Locate cells.
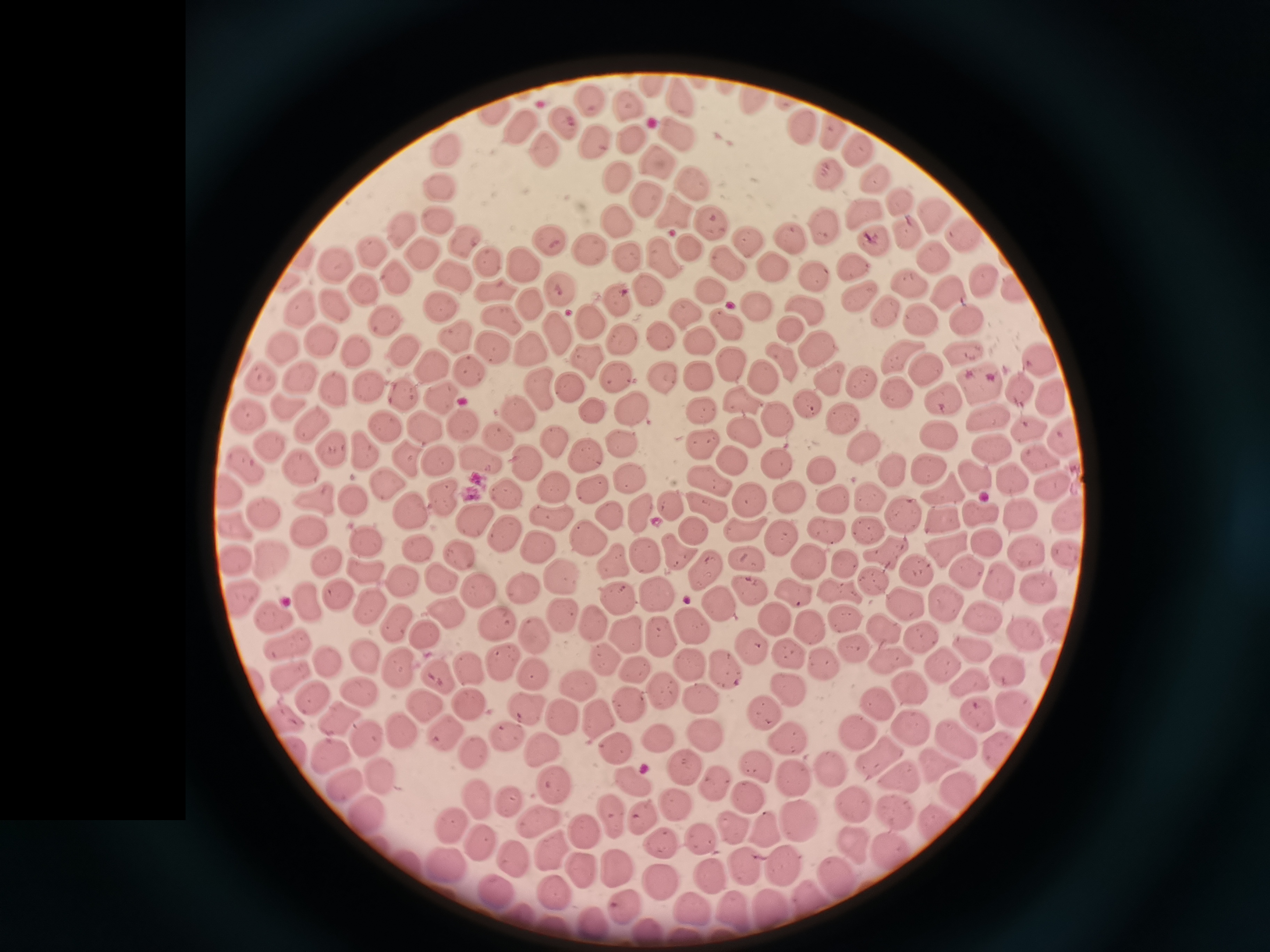

Approximate object centers, in pixels from the top-left corner.
Cells: (x=650, y=89), (x=684, y=99), (x=755, y=99), (x=594, y=104), (x=629, y=107), (x=493, y=111), (x=564, y=124), (x=521, y=125), (x=803, y=127), (x=833, y=132), (x=677, y=134), (x=633, y=137), (x=599, y=143), (x=856, y=150), (x=548, y=153), (x=444, y=156), (x=652, y=161), (x=828, y=174), (x=616, y=179), (x=875, y=180), (x=694, y=182), (x=439, y=190), (x=653, y=201), (x=898, y=201), (x=863, y=212), (x=675, y=213), (x=930, y=214), (x=438, y=222), (x=615, y=222), (x=710, y=223), (x=398, y=228), (x=828, y=228), (x=790, y=234), (x=964, y=234), (x=904, y=236), (x=459, y=241), (x=547, y=242), (x=749, y=242), (x=870, y=246), (x=686, y=247), (x=587, y=248), (x=369, y=252), (x=421, y=255), (x=625, y=256), (x=659, y=257), (x=933, y=257), (x=721, y=259), (x=487, y=261), (x=851, y=266), (x=332, y=267), (x=770, y=267), (x=815, y=272), (x=454, y=274), (x=393, y=279), (x=986, y=280), (x=911, y=283), (x=362, y=287), (x=498, y=290), (x=947, y=290), (x=1014, y=290), (x=709, y=291), (x=858, y=295), (x=807, y=303), (x=757, y=304), (x=300, y=308), (x=443, y=309), (x=683, y=310), (x=891, y=310), (x=380, y=319), (x=965, y=319), (x=922, y=320), (x=722, y=323), (x=785, y=326), (x=454, y=336), (x=317, y=339), (x=702, y=341), (x=283, y=347), (x=812, y=347), (x=490, y=349), (x=354, y=350), (x=900, y=350), (x=399, y=351), (x=963, y=354), (x=1036, y=357), (x=587, y=359), (x=781, y=360), (x=429, y=362), (x=730, y=363), (x=467, y=367), (x=924, y=369), (x=826, y=374), (x=295, y=375), (x=760, y=375), (x=614, y=377), (x=700, y=377), (x=261, y=378), (x=666, y=378), (x=863, y=379), (x=978, y=383), (x=367, y=384), (x=568, y=386), (x=1019, y=386), (x=333, y=389), (x=898, y=392), (x=938, y=392), (x=543, y=393), (x=1053, y=393), (x=404, y=394), (x=439, y=398), (x=743, y=401), (x=808, y=403), (x=287, y=405), (x=632, y=408), (x=592, y=412), (x=845, y=414), (x=516, y=415), (x=703, y=415), (x=247, y=416), (x=776, y=417), (x=989, y=418), (x=460, y=423), (x=314, y=424), (x=387, y=425), (x=424, y=425), (x=1029, y=426), (x=743, y=431), (x=937, y=434), (x=1065, y=434), (x=500, y=435), (x=555, y=438), (x=622, y=441), (x=704, y=443), (x=269, y=444), (x=862, y=445), (x=330, y=446), (x=989, y=446), (x=365, y=448), (x=583, y=454), (x=733, y=457), (x=1042, y=457), (x=436, y=458), (x=481, y=458), (x=296, y=460), (x=527, y=460), (x=406, y=461), (x=773, y=461), (x=931, y=465), (x=247, y=466), (x=893, y=471), (x=823, y=472), (x=977, y=472), (x=626, y=475), (x=1016, y=478), (x=707, y=480), (x=552, y=482), (x=384, y=483), (x=1051, y=483), (x=590, y=485), (x=229, y=489), (x=940, y=490), (x=504, y=493), (x=439, y=495), (x=872, y=496), (x=791, y=497), (x=319, y=500), (x=749, y=500), (x=833, y=500), (x=358, y=501), (x=671, y=504), (x=703, y=505), (x=640, y=509), (x=977, y=511), (x=1018, y=512), (x=264, y=513), (x=412, y=513), (x=1067, y=513), (x=608, y=514), (x=901, y=514), (x=944, y=516), (x=550, y=518), (x=469, y=519), (x=237, y=524), (x=825, y=526), (x=741, y=529), (x=309, y=530), (x=508, y=531), (x=866, y=532), (x=696, y=533), (x=586, y=535), (x=778, y=535), (x=985, y=544), (x=538, y=545), (x=369, y=546), (x=417, y=547), (x=1066, y=547), (x=943, y=548), (x=877, y=551), (x=459, y=552), (x=672, y=553), (x=1027, y=553), (x=642, y=554), (x=235, y=556), (x=270, y=556), (x=324, y=557), (x=745, y=558), (x=807, y=558), (x=612, y=560), (x=843, y=564), (x=965, y=569), (x=364, y=571), (x=917, y=571), (x=705, y=572), (x=556, y=578), (x=997, y=579), (x=441, y=580), (x=871, y=581), (x=400, y=582), (x=1031, y=585), (x=840, y=588), (x=476, y=590), (x=523, y=590), (x=794, y=591), (x=653, y=593), (x=750, y=593), (x=241, y=594), (x=345, y=596), (x=611, y=600), (x=313, y=603), (x=906, y=604), (x=949, y=604), (x=373, y=606), (x=718, y=606), (x=276, y=613), (x=564, y=613), (x=446, y=616), (x=844, y=616), (x=984, y=617), (x=589, y=619), (x=772, y=619), (x=1056, y=622), (x=394, y=623), (x=497, y=623), (x=690, y=623), (x=812, y=627), (x=883, y=628), (x=658, y=630), (x=624, y=633), (x=535, y=634), (x=423, y=635), (x=916, y=636), (x=1026, y=637), (x=288, y=645), (x=851, y=645), (x=971, y=646), (x=750, y=648), (x=786, y=652), (x=363, y=656), (x=887, y=656), (x=604, y=658), (x=499, y=659), (x=820, y=660), (x=691, y=662), (x=1052, y=662), (x=327, y=664), (x=395, y=665), (x=634, y=668), (x=943, y=668), (x=469, y=670), (x=533, y=671), (x=725, y=671), (x=1008, y=671), (x=290, y=673), (x=431, y=673), (x=970, y=682), (x=577, y=683), (x=908, y=683), (x=786, y=685), (x=662, y=687), (x=360, y=693), (x=313, y=695), (x=626, y=699), (x=700, y=699), (x=880, y=699), (x=421, y=704), (x=469, y=704), (x=526, y=707), (x=1012, y=709), (x=975, y=712), (x=561, y=713), (x=765, y=713), (x=598, y=714), (x=286, y=716), (x=338, y=719), (x=399, y=728), (x=910, y=730), (x=445, y=733), (x=502, y=734), (x=858, y=734), (x=657, y=735), (x=705, y=735), (x=784, y=736), (x=954, y=739), (x=368, y=743), (x=613, y=745), (x=994, y=748), (x=543, y=750), (x=476, y=752), (x=332, y=756), (x=876, y=756), (x=679, y=763), (x=935, y=763), (x=762, y=766), (x=832, y=768), (x=381, y=774), (x=898, y=775), (x=791, y=777), (x=631, y=780), (x=340, y=783), (x=550, y=783), (x=957, y=791), (x=474, y=795), (x=507, y=797), (x=746, y=797), (x=671, y=802), (x=849, y=803), (x=362, y=810), (x=610, y=811), (x=641, y=815), (x=891, y=815), (x=795, y=818), (x=535, y=819), (x=939, y=821), (x=449, y=825), (x=762, y=826), (x=731, y=829), (x=584, y=830), (x=700, y=834), (x=477, y=840), (x=856, y=843), (x=658, y=845), (x=889, y=846), (x=545, y=850), (x=512, y=859), (x=406, y=861), (x=440, y=865), (x=580, y=867), (x=616, y=867), (x=743, y=867), (x=782, y=867), (x=710, y=876), (x=839, y=879), (x=659, y=881), (x=497, y=892), (x=555, y=897), (x=803, y=899), (x=626, y=904), (x=768, y=906), (x=693, y=907), (x=730, y=909), (x=523, y=914), (x=595, y=922), (x=555, y=926).

{
  "field_of_view": "single",
  "image_size": "1270×952 pixels",
  "capture": "smartphone camera at the microscope eyepiece",
  "preparation": "thin blood film",
  "stain": "Giemsa"
}